Give the preparation type.
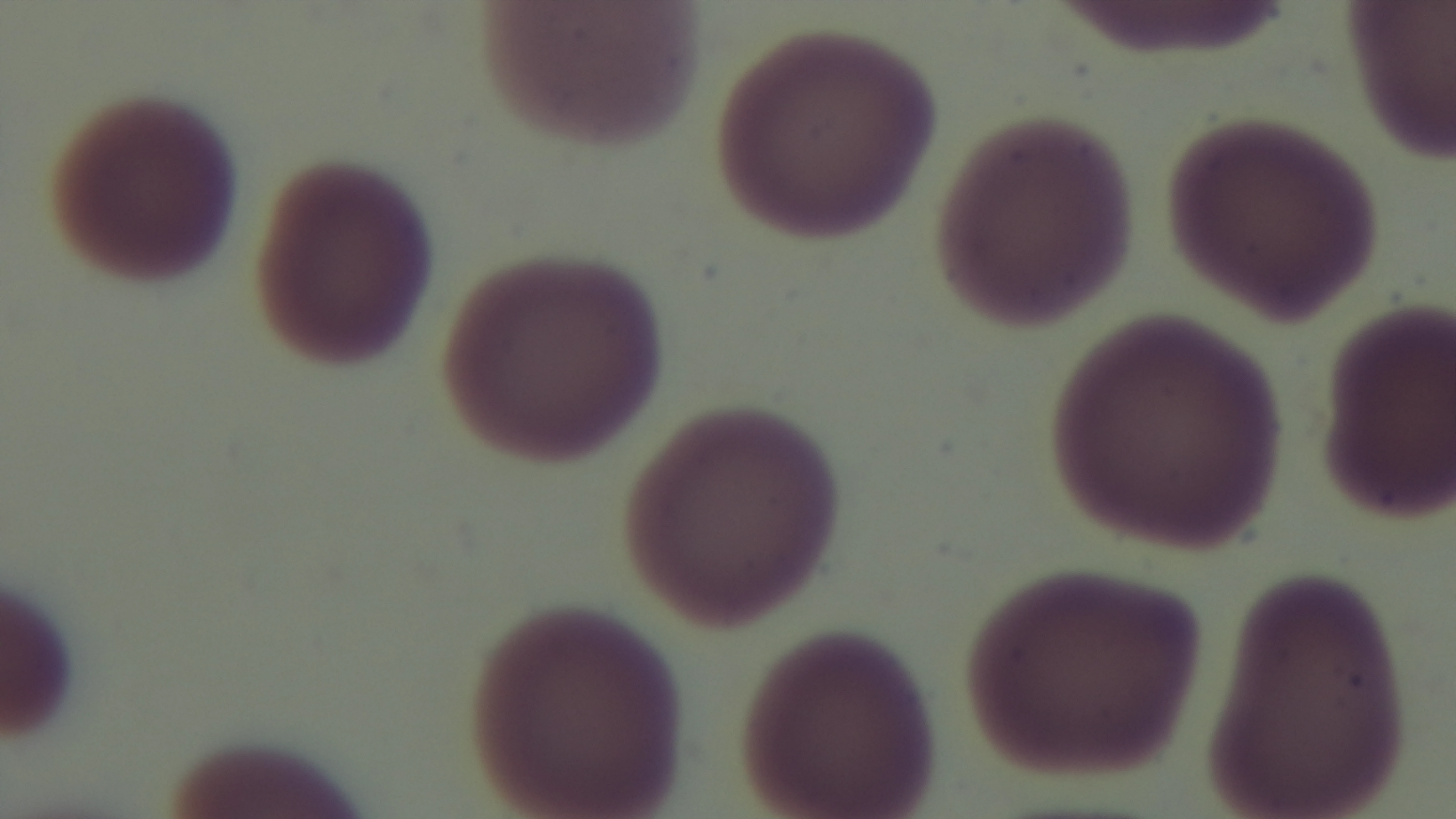
It is a thin blood film.

One field from the slide. 100x oil-immersion objective. Giemsa-stained. Captured with a mounted 4K digital camera. Light microscopy. Malaria status: negative.